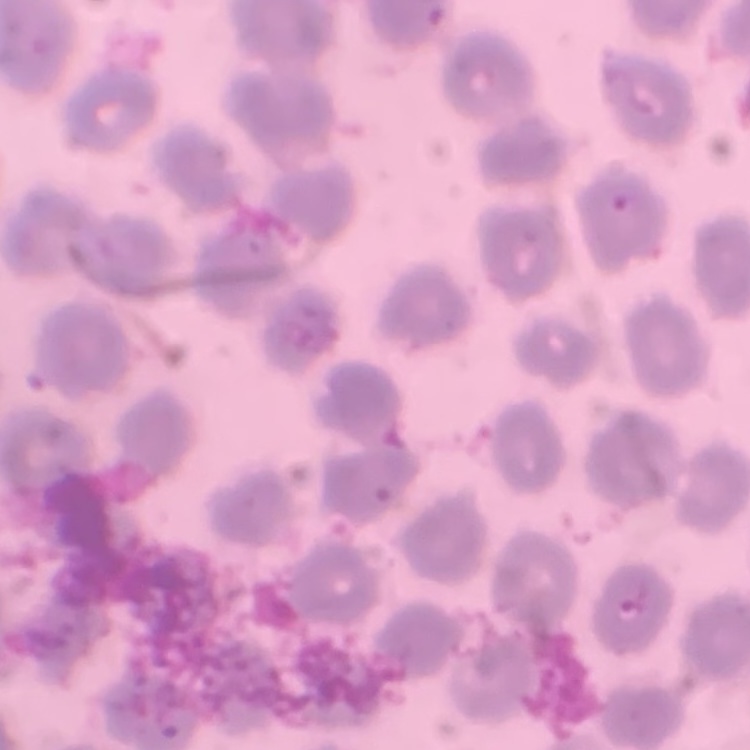
The erythrocytes exhibit no rouleaux formation. Thin peripheral smear. Field's or Giemsa stain. One tile cut from a larger photomicrograph.